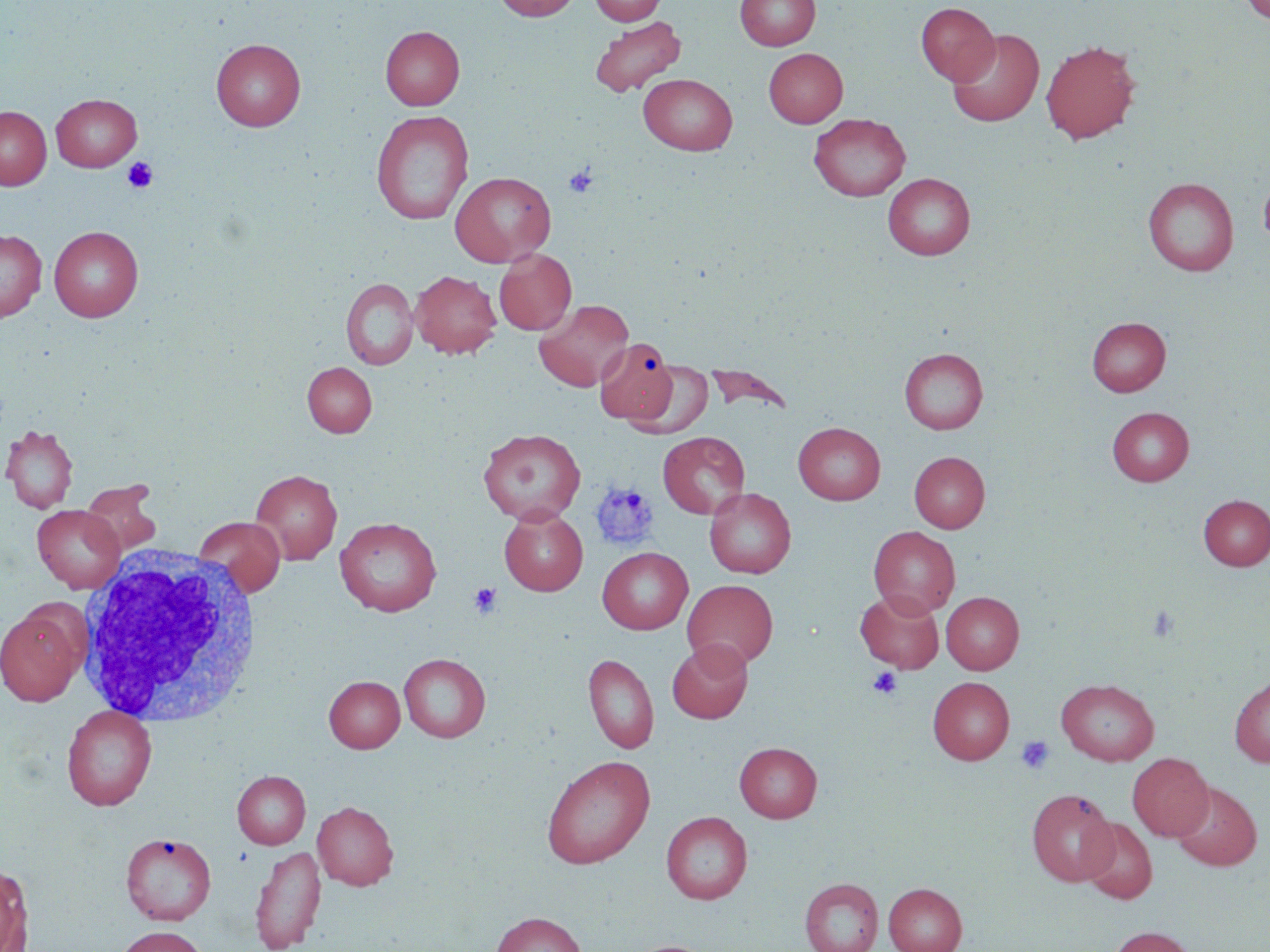
Summary:
  - Coordinate format: approximate bounding boxes as (x1, y1, x2, y2) in pixels
  - White blood cell locations: (73, 545, 263, 731)
  - Uninfected red blood cell locations: (493, 0, 580, 21), (589, 0, 667, 25), (735, 0, 820, 51), (1239, 0, 1270, 24), (916, 2, 1000, 85), (589, 16, 686, 99), (380, 25, 464, 110), (948, 28, 1045, 127), (211, 38, 306, 131), (1041, 39, 1141, 144), (764, 48, 848, 127), (639, 73, 737, 155), (51, 93, 142, 171), (0, 106, 51, 190), (371, 110, 474, 225), (810, 113, 911, 201), (450, 171, 556, 267), (1258, 171, 1270, 250), (883, 172, 975, 260), (1143, 177, 1238, 276), (49, 226, 144, 322), (0, 229, 47, 322), (494, 248, 576, 335), (410, 270, 502, 358), (340, 277, 418, 370), (534, 299, 633, 392), (1088, 317, 1170, 396), (595, 339, 676, 424), (899, 348, 988, 434), (302, 361, 377, 438), (626, 361, 713, 438), (706, 363, 794, 415), (1107, 407, 1194, 486), (793, 422, 885, 505), (1, 424, 79, 513), (478, 428, 585, 525), (658, 432, 749, 518), (909, 451, 990, 533), (250, 469, 343, 564), (78, 480, 162, 554), (705, 488, 796, 579), (1198, 494, 1270, 571), (32, 504, 126, 592), (500, 508, 588, 596), (194, 516, 285, 597), (335, 517, 441, 616), (868, 526, 961, 617), (597, 547, 693, 634), (682, 579, 778, 669), (855, 590, 944, 673), (941, 591, 1024, 674), (0, 607, 86, 705), (668, 641, 752, 723), (399, 653, 491, 742), (583, 654, 658, 754), (1230, 674, 1270, 768), (324, 675, 405, 752), (928, 677, 1014, 764), (1056, 678, 1159, 765), (61, 705, 157, 811), (734, 741, 822, 822), (1127, 752, 1213, 841), (542, 755, 655, 868), (232, 771, 310, 849), (1172, 782, 1262, 871), (1026, 789, 1116, 885), (312, 800, 398, 890), (661, 811, 752, 904), (1080, 817, 1157, 904), (121, 832, 216, 925), (250, 844, 326, 951), (0, 863, 33, 952), (800, 878, 883, 952), (884, 883, 967, 952), (490, 912, 585, 952), (117, 926, 207, 952), (1108, 926, 1195, 952), (622, 940, 717, 952)
  - Platelet locations: (122, 156, 159, 194), (564, 165, 598, 199), (592, 485, 658, 549), (469, 582, 502, 618), (1145, 604, 1181, 643), (868, 666, 902, 698), (1016, 736, 1054, 774)
  - Slide-level diagnosis: no evidence of blood parasites
  - Modality: light microscopy
  - Field of view: one of a larger specimen
  - Stain: May-Grünwald-Giemsa
  - Magnification: 1000x
  - Image size: 1270×952 pixels
  - Preparation: thin blood film